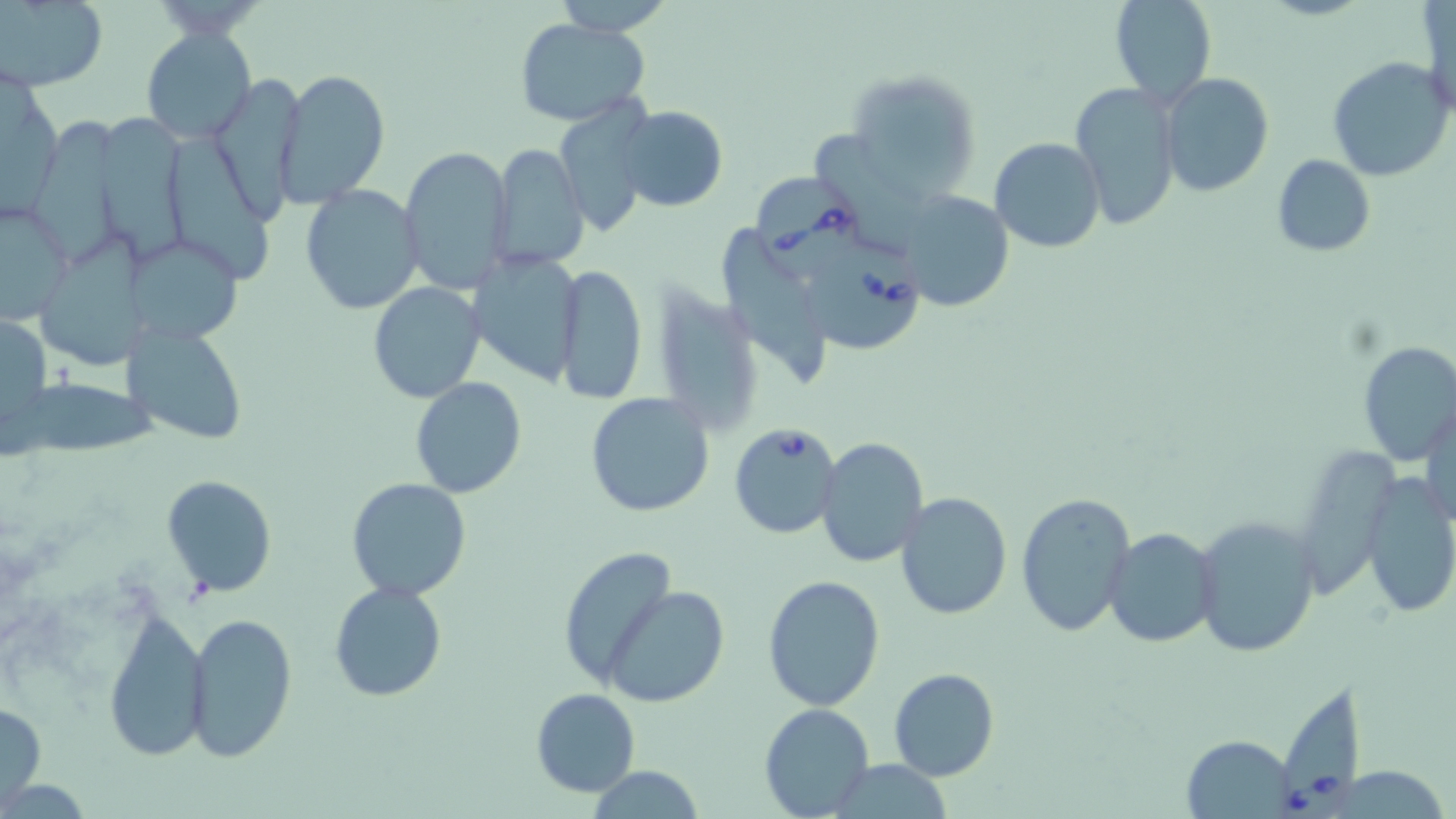
Summary:
  - Coordinate format: approximate bounding boxes as (x1, y1, x2, y2) in pixels
  - Babesia divergens-infected red blood cell locations: (750, 173, 861, 273), (803, 241, 929, 354), (729, 422, 843, 539), (1277, 683, 1371, 819)
  - Uninfected red blood cell locations: (0, 0, 107, 89), (550, 0, 675, 36), (1110, 0, 1216, 104), (515, 17, 652, 127), (142, 26, 255, 143), (1327, 56, 1454, 182), (274, 67, 391, 208), (847, 67, 985, 196), (1159, 72, 1274, 196), (207, 74, 307, 218), (1069, 83, 1181, 231), (553, 100, 660, 236), (617, 106, 727, 212), (32, 109, 128, 264), (101, 110, 188, 262), (162, 134, 277, 287), (989, 138, 1106, 254), (485, 141, 591, 272), (399, 146, 516, 297), (1271, 155, 1376, 257), (300, 185, 425, 315), (898, 191, 1014, 310), (0, 199, 75, 328), (725, 222, 829, 387), (131, 229, 246, 345), (463, 250, 584, 384), (554, 262, 647, 405), (368, 282, 486, 403), (0, 311, 51, 445), (128, 321, 248, 444), (1355, 340, 1456, 465), (11, 376, 153, 455), (409, 376, 526, 499), (586, 391, 714, 517), (1423, 402, 1455, 530), (813, 436, 930, 569), (160, 474, 278, 598), (1360, 475, 1456, 620), (346, 478, 473, 601), (1017, 491, 1138, 637), (896, 492, 1013, 619), (1193, 514, 1321, 658), (1102, 527, 1220, 649), (558, 546, 677, 687), (761, 576, 886, 711), (328, 582, 448, 702), (604, 586, 730, 706), (101, 609, 211, 762), (184, 611, 297, 762), (887, 668, 999, 780), (531, 688, 640, 797), (0, 700, 46, 808), (757, 704, 874, 817), (1183, 734, 1297, 818), (583, 766, 705, 819)
  - Slide-level diagnosis: Babesia divergens
  - Stain: May-Grünwald-Giemsa
  - Preparation: thin blood smear
  - Image size: 1456×819 pixels
  - Magnification: 1000x
  - Modality: optical microscopy
  - Field of view: single